Give the preparation type.
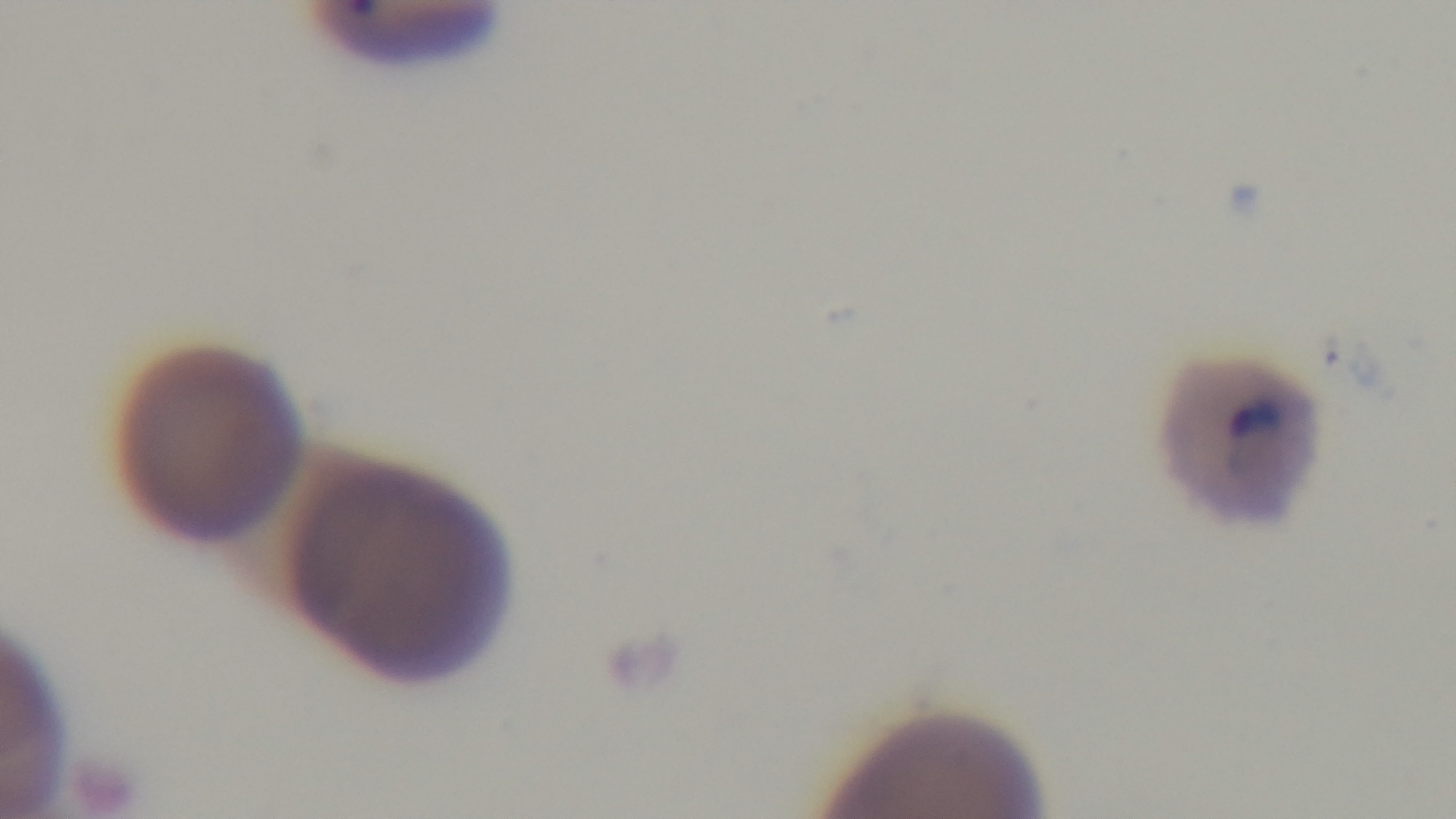
Thin.

modality = light microscopy
capture = mounted 4K digital camera
malaria status = positive
objective = 100x oil immersion
field of view = one from the slide
stain = Giemsa